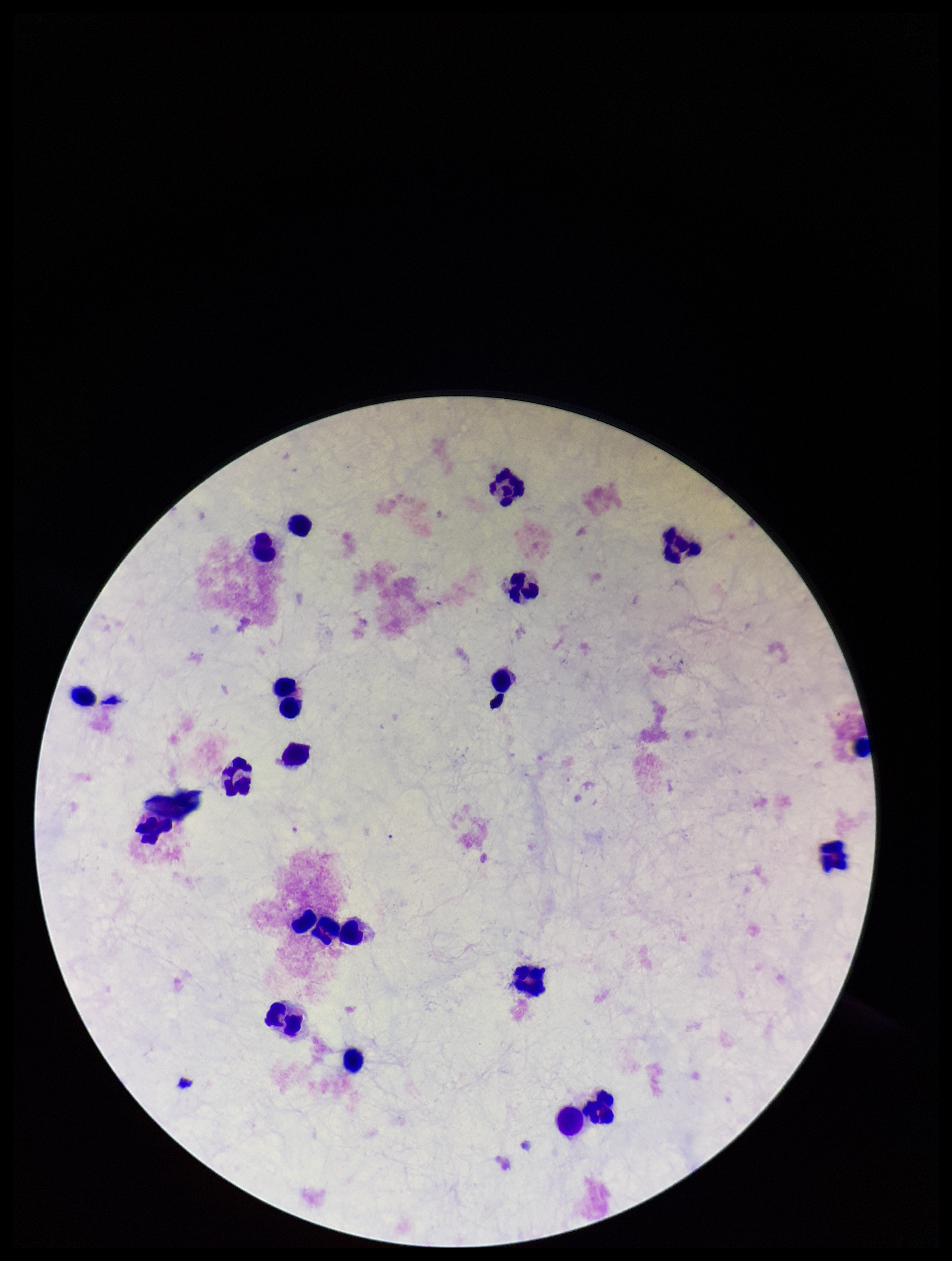 Plasmodium parasites: none identified. Smartphone photograph taken through the eyepiece of a microscope. Single field of view. Patient malaria status: negative. Preparation: thick blood smear. Image is 952×1261 pixels. Leukocyte count: 21. Giemsa stain. Parasite count: 0.